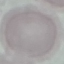

malaria_status: uninfected
stain: Giemsa
image_type: cell patch, automatically extracted from a larger field of view and resized to 64 × 64 pixels
preparation: thin blood film
capture: smartphone camera at the microscope eyepiece